State which parasite is depicted.
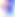
Toxoplasma gondii.

modality = micrograph
magnification = 400x